Point out each leukocyte.
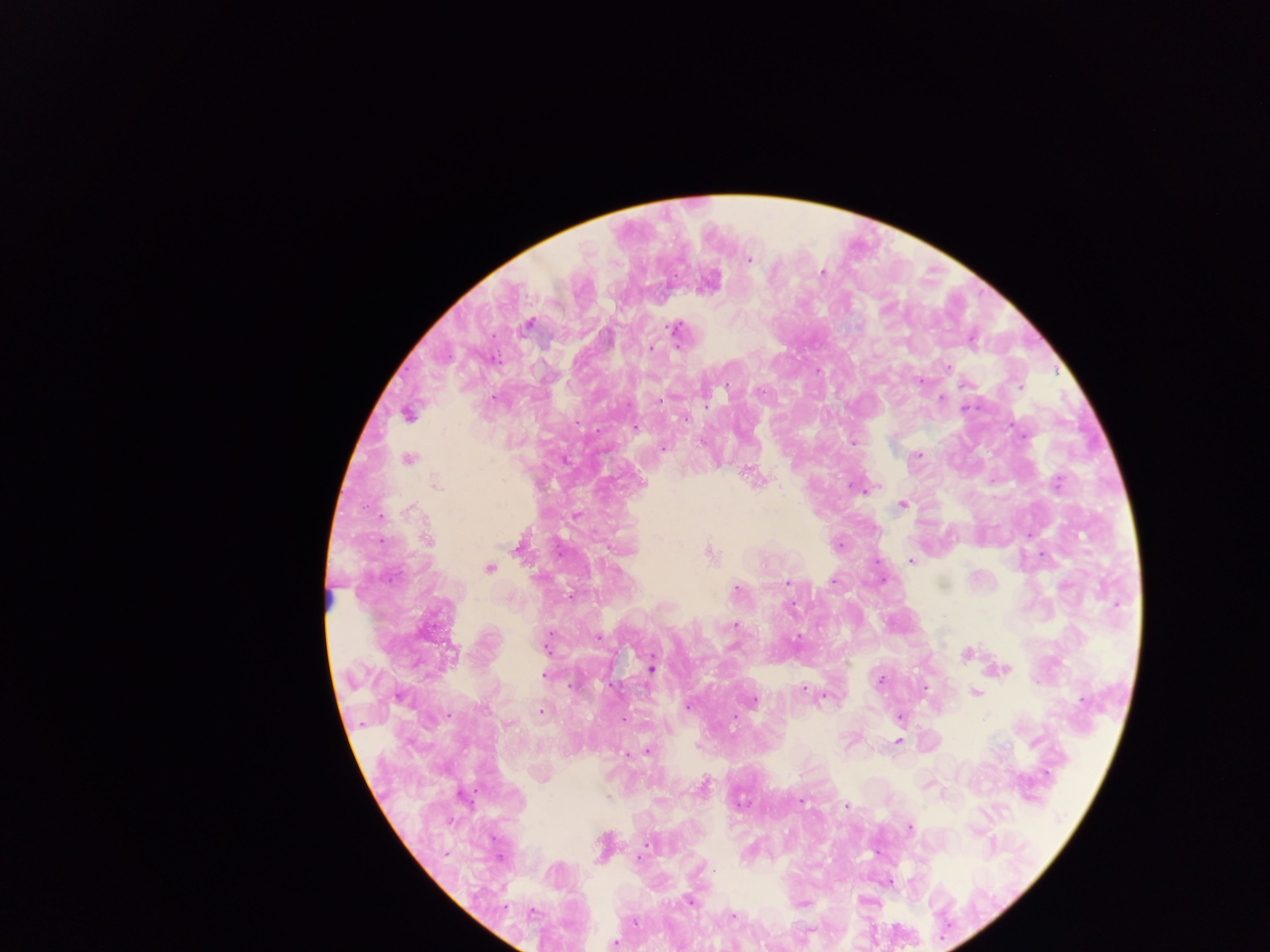
Approximate centers as [x, y] in pixels.
Leukocytes: [327, 600].

image size = 1270×952 pixels
preparation = thick blood film
country = Ghana
Plasmodium parasite locations = approximate centers as [x, y] in pixels: [748, 260], [822, 273], [709, 283], [527, 325], [674, 328], [651, 348], [948, 367], [920, 381], [966, 384], [1020, 387], [940, 397], [494, 399], [968, 408], [407, 415], [684, 418], [853, 443], [664, 449], [918, 455], [407, 459], [1057, 482], [435, 483], [855, 486], [902, 505], [412, 510], [380, 516], [428, 540], [518, 546], [710, 553], [910, 561], [489, 568], [833, 579], [787, 583], [736, 589], [791, 607], [735, 625], [599, 638], [797, 638], [547, 644], [453, 651], [967, 654], [652, 669], [1006, 670], [545, 675], [880, 682], [804, 689], [975, 692], [822, 696], [399, 698], [754, 701], [688, 706], [541, 712], [899, 717], [510, 724], [899, 742], [696, 745], [648, 751], [626, 755], [705, 784], [800, 801], [847, 807], [910, 827], [647, 845], [639, 856], [689, 901], [803, 903], [532, 913], [731, 917], [633, 922], [614, 943]
field of view = single
capture = mobile-phone photograph through a microscope